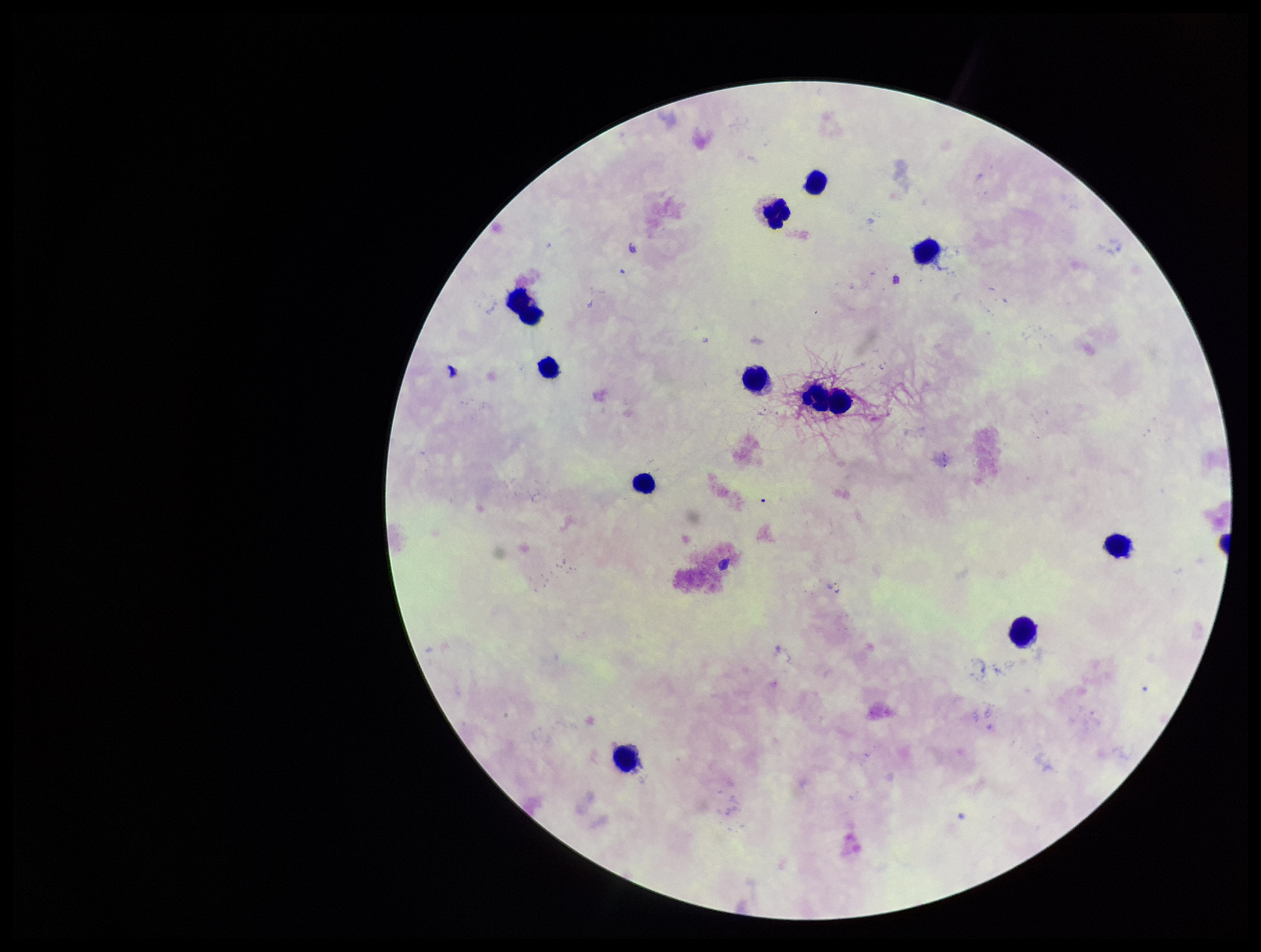

{
  "preparation": "thick smear",
  "capture": "smartphone photograph through the microscope eyepiece",
  "patient_malaria_status": "negative",
  "image_size": "1261×952 pixels",
  "stain": "Giemsa",
  "parasite_count": 0,
  "plasmodium_parasites": "none detected",
  "leukocyte_count": 12,
  "field_of_view": "one from this slide"
}